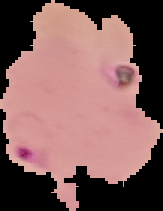
{
  "result": "Plasmodium parasites identified",
  "image_size": "163×211 pixels",
  "image_type": "segmented cell region with the area outside set to black",
  "preparation": "thin blood film"
}